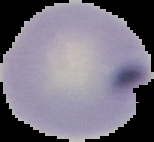
preparation = thin blood film
result = no Plasmodium parasites seen
image size = 154×142 pixels
image type = segmented cell region with the area outside set to black